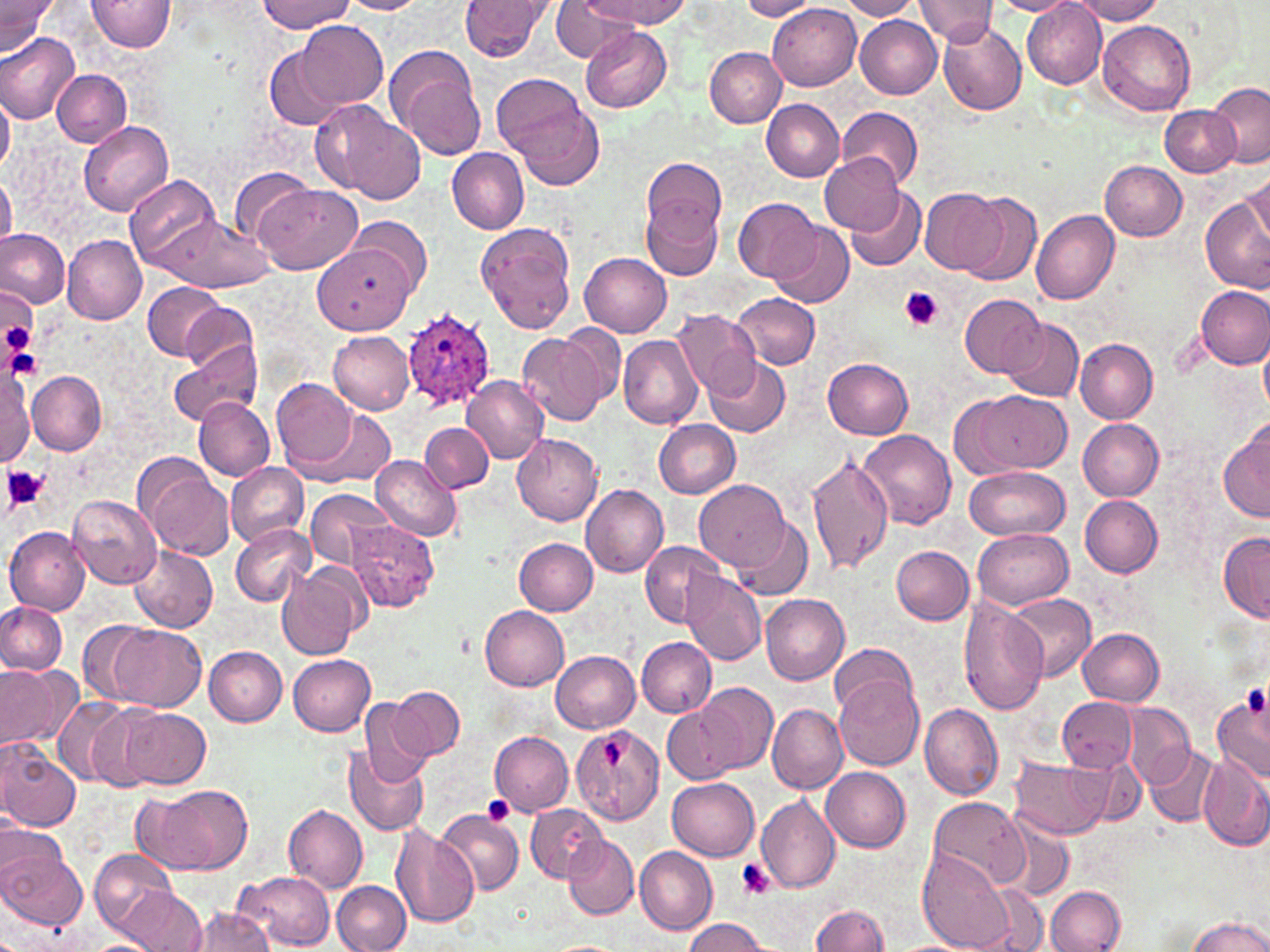

slide_level_diagnosis: Plasmodium ovale
image_size: 1270×952 pixels
field_of_view: one of a larger specimen
uninfected_red_blood_cell_locations: 'approximate bounding boxes as (x1, y1, x2, y2) in pixels: (0, 0, 56, 56), (89, 0, 177, 51), (256, 0, 353, 32), (339, 0, 428, 14), (457, 0, 556, 61), (584, 0, 689, 29), (838, 0, 921, 20), (917, 0, 999, 44), (1071, 0, 1167, 24), (552, 1, 640, 62), (738, 1, 819, 20), (991, 1, 1081, 16), (768, 3, 861, 91), (1022, 4, 1107, 87), (855, 16, 942, 99), (297, 20, 387, 112), (1098, 20, 1196, 116), (936, 21, 1026, 114), (581, 27, 673, 113), (0, 30, 80, 125), (265, 45, 352, 130), (387, 47, 487, 162), (704, 47, 786, 127), (51, 69, 131, 146), (492, 75, 603, 188), (1204, 80, 1269, 166), (0, 94, 14, 174), (760, 98, 844, 181), (314, 102, 427, 204), (1159, 103, 1241, 177), (837, 105, 924, 189), (77, 121, 173, 217), (446, 148, 529, 234), (819, 153, 904, 234), (642, 157, 728, 246), (1100, 160, 1187, 241), (229, 167, 318, 242), (1243, 169, 1270, 250), (0, 174, 16, 251), (126, 174, 221, 271), (254, 182, 363, 275), (844, 188, 927, 272), (921, 188, 1005, 275), (640, 193, 724, 280), (959, 193, 1042, 285), (733, 197, 822, 282), (1202, 198, 1270, 292), (1032, 209, 1120, 305), (157, 214, 273, 293), (350, 217, 432, 297), (477, 221, 578, 334), (770, 222, 854, 308), (0, 227, 69, 308), (63, 236, 147, 325), (313, 247, 412, 334), (581, 253, 672, 337), (142, 283, 225, 359), (1195, 285, 1270, 369), (1, 291, 37, 365), (731, 293, 821, 370), (959, 293, 1046, 376), (181, 302, 259, 375), (672, 310, 762, 397), (1000, 317, 1085, 403), (562, 324, 625, 403), (328, 331, 415, 414), (518, 333, 607, 425), (618, 334, 703, 429), (1260, 336, 1269, 417), (1074, 338, 1158, 422), (168, 339, 263, 427), (704, 355, 791, 437), (822, 358, 914, 439), (0, 367, 34, 467), (0, 371, 76, 458), (29, 371, 107, 454), (460, 374, 549, 464), (273, 378, 359, 473), (959, 390, 1069, 477), (193, 398, 274, 481), (297, 407, 397, 488), (654, 419, 741, 499), (1078, 419, 1164, 502), (419, 421, 493, 493), (1218, 422, 1269, 524), (858, 430, 957, 529), (512, 433, 604, 526), (807, 454, 894, 575), (371, 455, 461, 542), (225, 461, 308, 546), (142, 466, 235, 560), (962, 466, 1070, 539), (696, 479, 791, 571), (581, 485, 669, 577), (306, 488, 394, 572), (1079, 493, 1163, 578), (68, 495, 161, 587), (735, 517, 813, 600), (344, 520, 439, 612), (229, 523, 316, 609), (974, 525, 1074, 609), (5, 528, 90, 615), (1218, 533, 1270, 623), (514, 538, 597, 615), (639, 541, 726, 627), (890, 545, 973, 624), (130, 546, 217, 632), (279, 562, 365, 660), (680, 568, 766, 666), (1007, 593, 1096, 682), (760, 594, 849, 683), (959, 598, 1049, 715), (0, 603, 68, 676), (480, 605, 570, 691), (77, 619, 161, 706), (101, 623, 207, 711), (1077, 628, 1164, 706), (636, 637, 716, 717), (828, 644, 918, 717), (205, 646, 287, 726), (551, 651, 641, 733), (287, 654, 375, 736), (0, 662, 81, 755), (834, 679, 924, 768), (696, 682, 778, 772), (388, 686, 464, 760), (1213, 692, 1270, 786), (359, 693, 435, 786), (49, 694, 135, 787), (1058, 697, 1137, 771), (766, 702, 847, 795), (919, 703, 1004, 800), (1120, 703, 1195, 788), (89, 705, 169, 790), (662, 705, 741, 784), (120, 708, 212, 789), (571, 718, 664, 827), (489, 729, 574, 816), (0, 742, 81, 831), (343, 744, 430, 835), (1144, 745, 1223, 827), (1198, 754, 1270, 850), (1010, 756, 1114, 840), (820, 767, 910, 851), (666, 777, 759, 861), (132, 785, 252, 876), (755, 795, 840, 895), (929, 796, 1027, 888), (527, 803, 606, 881), (283, 804, 369, 893), (437, 808, 525, 897), (995, 815, 1073, 902), (391, 825, 480, 929), (0, 835, 85, 929), (564, 835, 638, 920), (634, 846, 718, 935), (90, 847, 178, 941), (919, 847, 1015, 951), (235, 870, 335, 951), (331, 881, 411, 952), (976, 883, 1050, 952), (116, 886, 207, 952), (1046, 886, 1126, 951), (810, 903, 891, 951), (187, 908, 274, 952), (1185, 916, 1270, 952), (682, 918, 771, 952), (543, 939, 626, 952)'
plasmodium_ovale_infected_red_blood_cell_locations: 'approximate bounding boxes as (x1, y1, x2, y2) in pixels: (403, 310, 497, 417)'
stain: May-Grünwald-Giemsa
modality: optical microscopy
platelet_locations: 'approximate bounding boxes as (x1, y1, x2, y2) in pixels: (898, 287, 943, 332), (1, 310, 39, 366), (3, 335, 42, 379), (3, 465, 48, 510), (1242, 685, 1268, 718), (599, 740, 631, 770), (481, 796, 514, 826), (737, 859, 776, 900)'
magnification: 1000x
preparation: thin blood smear